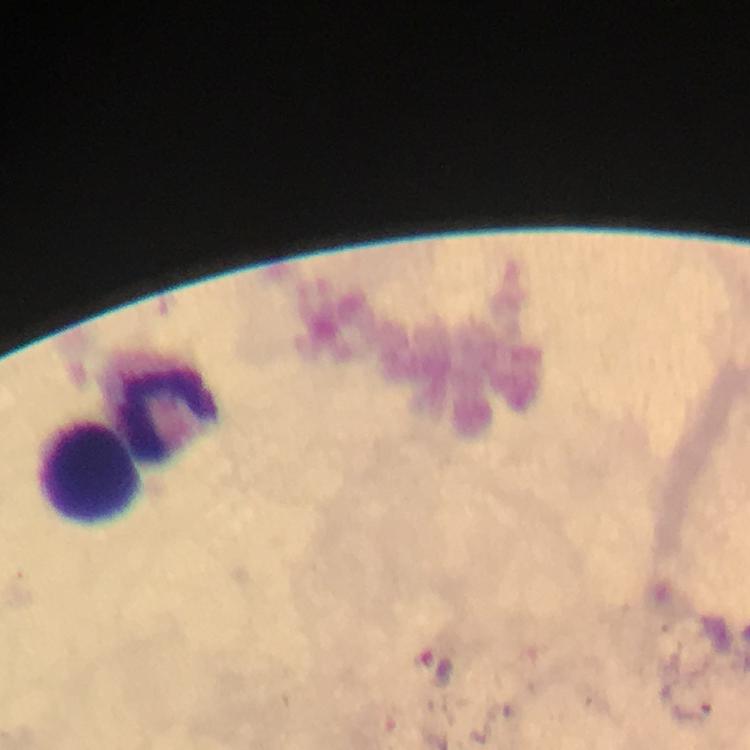
Approximate object centers, in pixels from the top-left corner. Leukocyte locations: (x=162, y=413), (x=90, y=473). At 100x magnification. Giemsa-stained preparation. Thick smear. Image is 750×750 pixels. Immersion oil was used. From a malaria diagnostic workup. Photographed with a smartphone mounted on the microscope. Cropped region of a single field of view. Plasmodium parasites: none detected.